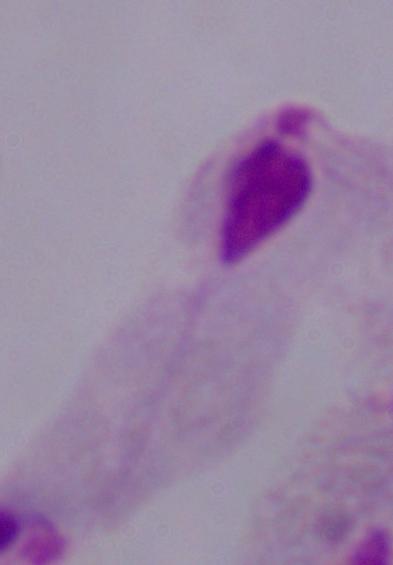

Captured at 1000x magnification. Photomicrograph. A trichomonad is seen.